Report the malaria status of this cell.
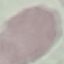
It is uninfected.

Photographed with a smartphone camera at the microscope eyepiece. Automatically extracted cell patch, resized to 64 × 64 pixels. Thin blood film. Giemsa stain.